Outline each Plasmodium falciparum-infected red blood cell.
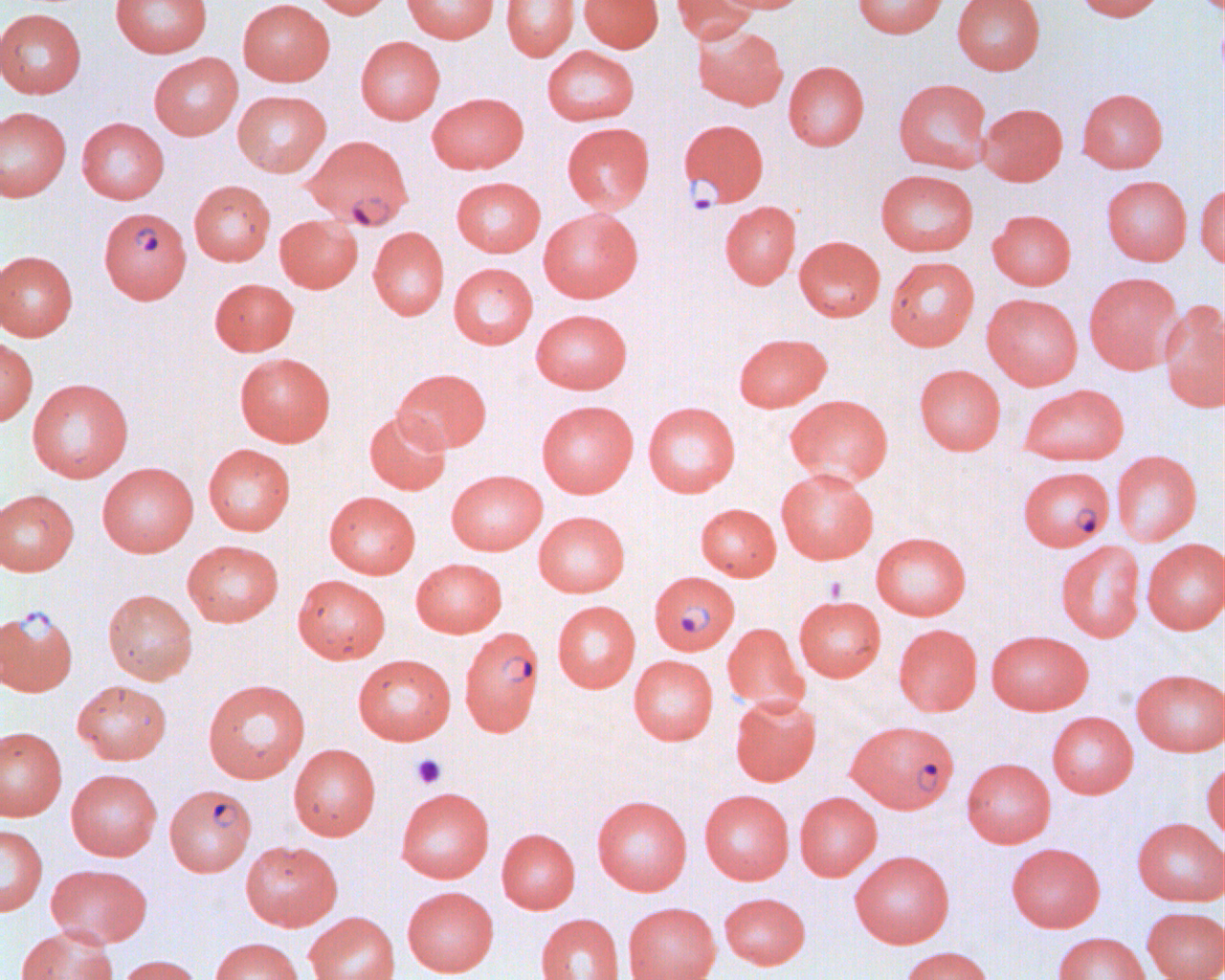
Approximate bounding boxes as named x1/y1/x2/y2 corners in pixels.
Plasmodium falciparum-infected red blood cells: (x1=679, y1=118, x2=769, y2=206), (x1=299, y1=131, x2=409, y2=225), (x1=99, y1=207, x2=191, y2=304), (x1=1017, y1=465, x2=1115, y2=551), (x1=648, y1=571, x2=740, y2=655), (x1=0, y1=606, x2=78, y2=697), (x1=465, y1=630, x2=551, y2=740), (x1=845, y1=719, x2=959, y2=813), (x1=164, y1=784, x2=256, y2=876).

slide-level diagnosis = Plasmodium falciparum
magnification = 1000x
modality = light microscopy
uninfected red blood cell locations = approximate bounding boxes as named x1/y1/x2/y2 corners in pixels: (x1=111, y1=0, x2=212, y2=57), (x1=237, y1=0, x2=334, y2=86), (x1=308, y1=0, x2=393, y2=19), (x1=402, y1=0, x2=498, y2=43), (x1=501, y1=0, x2=579, y2=61), (x1=579, y1=0, x2=664, y2=52), (x1=671, y1=0, x2=757, y2=45), (x1=715, y1=0, x2=813, y2=13), (x1=852, y1=0, x2=948, y2=38), (x1=952, y1=0, x2=1045, y2=75), (x1=1071, y1=0, x2=1166, y2=22), (x1=1195, y1=0, x2=1221, y2=16), (x1=0, y1=9, x2=86, y2=98), (x1=692, y1=24, x2=788, y2=110), (x1=356, y1=36, x2=445, y2=124), (x1=541, y1=46, x2=640, y2=125), (x1=149, y1=52, x2=242, y2=140), (x1=783, y1=61, x2=869, y2=150), (x1=893, y1=78, x2=993, y2=173), (x1=1077, y1=88, x2=1168, y2=173), (x1=232, y1=90, x2=331, y2=177), (x1=427, y1=92, x2=528, y2=174), (x1=978, y1=103, x2=1068, y2=186), (x1=0, y1=106, x2=71, y2=201), (x1=76, y1=117, x2=169, y2=204), (x1=561, y1=122, x2=655, y2=213), (x1=875, y1=169, x2=978, y2=256), (x1=1100, y1=174, x2=1191, y2=266), (x1=450, y1=176, x2=545, y2=257), (x1=189, y1=179, x2=275, y2=265), (x1=1196, y1=183, x2=1223, y2=269), (x1=719, y1=200, x2=801, y2=289), (x1=538, y1=207, x2=643, y2=303), (x1=987, y1=209, x2=1076, y2=290), (x1=275, y1=214, x2=362, y2=292), (x1=367, y1=226, x2=449, y2=320), (x1=794, y1=236, x2=885, y2=321), (x1=795, y1=243, x2=978, y2=330), (x1=0, y1=250, x2=78, y2=341), (x1=884, y1=256, x2=979, y2=351), (x1=448, y1=262, x2=538, y2=349), (x1=1084, y1=272, x2=1183, y2=375), (x1=209, y1=278, x2=298, y2=356), (x1=981, y1=293, x2=1083, y2=389), (x1=1160, y1=300, x2=1225, y2=413), (x1=530, y1=309, x2=633, y2=393), (x1=733, y1=333, x2=832, y2=412), (x1=0, y1=336, x2=38, y2=426), (x1=234, y1=352, x2=336, y2=446), (x1=914, y1=364, x2=1005, y2=455), (x1=393, y1=368, x2=491, y2=453), (x1=27, y1=378, x2=134, y2=482), (x1=1019, y1=383, x2=1129, y2=466), (x1=784, y1=394, x2=894, y2=486), (x1=536, y1=400, x2=638, y2=497), (x1=642, y1=401, x2=741, y2=497), (x1=364, y1=410, x2=451, y2=495), (x1=203, y1=443, x2=296, y2=535), (x1=1111, y1=449, x2=1202, y2=546), (x1=97, y1=462, x2=198, y2=557), (x1=775, y1=467, x2=879, y2=564), (x1=446, y1=470, x2=547, y2=555), (x1=0, y1=488, x2=79, y2=575), (x1=324, y1=491, x2=421, y2=578), (x1=696, y1=503, x2=781, y2=580), (x1=533, y1=511, x2=630, y2=597), (x1=870, y1=531, x2=971, y2=620), (x1=1141, y1=538, x2=1225, y2=634), (x1=182, y1=540, x2=284, y2=626), (x1=1056, y1=540, x2=1145, y2=642), (x1=410, y1=558, x2=507, y2=637), (x1=292, y1=574, x2=391, y2=663), (x1=102, y1=589, x2=198, y2=684), (x1=794, y1=596, x2=886, y2=681), (x1=552, y1=600, x2=640, y2=692), (x1=722, y1=622, x2=808, y2=711), (x1=893, y1=623, x2=983, y2=716), (x1=986, y1=629, x2=1092, y2=715), (x1=352, y1=653, x2=456, y2=744), (x1=628, y1=655, x2=718, y2=745), (x1=1131, y1=668, x2=1225, y2=756), (x1=202, y1=678, x2=310, y2=783), (x1=72, y1=679, x2=171, y2=764), (x1=730, y1=693, x2=821, y2=786), (x1=1046, y1=711, x2=1138, y2=798), (x1=0, y1=726, x2=67, y2=821), (x1=288, y1=743, x2=381, y2=840), (x1=962, y1=758, x2=1056, y2=847), (x1=1202, y1=759, x2=1225, y2=846), (x1=66, y1=768, x2=162, y2=860), (x1=395, y1=787, x2=494, y2=883), (x1=699, y1=789, x2=794, y2=884), (x1=794, y1=791, x2=882, y2=880), (x1=591, y1=795, x2=693, y2=895), (x1=1132, y1=817, x2=1225, y2=906), (x1=0, y1=824, x2=47, y2=916), (x1=496, y1=828, x2=580, y2=913), (x1=240, y1=840, x2=342, y2=930), (x1=1006, y1=843, x2=1105, y2=932), (x1=849, y1=850, x2=954, y2=948), (x1=46, y1=863, x2=152, y2=947), (x1=402, y1=886, x2=499, y2=976), (x1=719, y1=892, x2=811, y2=969), (x1=623, y1=902, x2=720, y2=980), (x1=1141, y1=906, x2=1225, y2=980), (x1=304, y1=911, x2=400, y2=980), (x1=536, y1=913, x2=624, y2=980), (x1=15, y1=925, x2=118, y2=980), (x1=1053, y1=932, x2=1149, y2=980), (x1=210, y1=937, x2=303, y2=980), (x1=899, y1=946, x2=995, y2=980), (x1=116, y1=954, x2=201, y2=980)
preparation = thin blood film
platelet locations = approximate bounding boxes as named x1/y1/x2/y2 corners in pixels: (x1=410, y1=753, x2=446, y2=789)
image size = 1225×980 pixels
field of view = single